Classify this cell by malaria status.
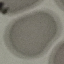
Uninfected.

stain = Giemsa
capture = smartphone camera at the microscope eyepiece
preparation = thin blood smear
image type = cell patch, automatically extracted from a larger field of view and resized to 64 × 64 pixels